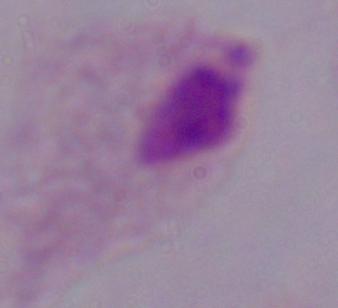
{
  "modality": "micrograph",
  "magnification": "1000x",
  "identification": "trichomonad"
}